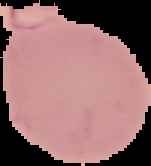
{
  "preparation": "thin blood smear",
  "image_size": "151×166 pixels",
  "image_type": "segmented cell region with the area outside set to black",
  "result": "malaria parasites detected"
}